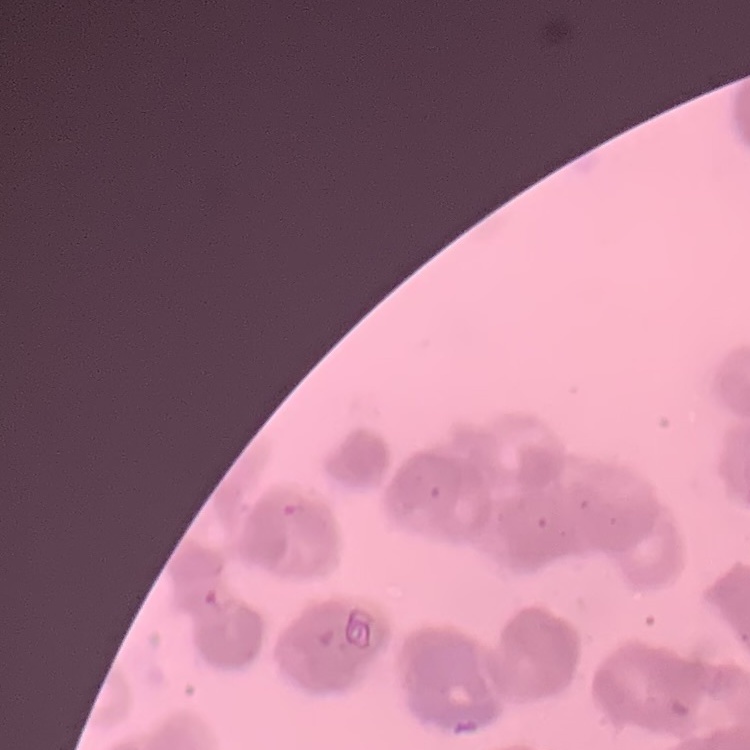
The red blood cells show rouleaux formation. Thin peripheral smear. Stained with either Field's or Giemsa. Square crop of a larger photomicrograph.